Point out each leukocyte.
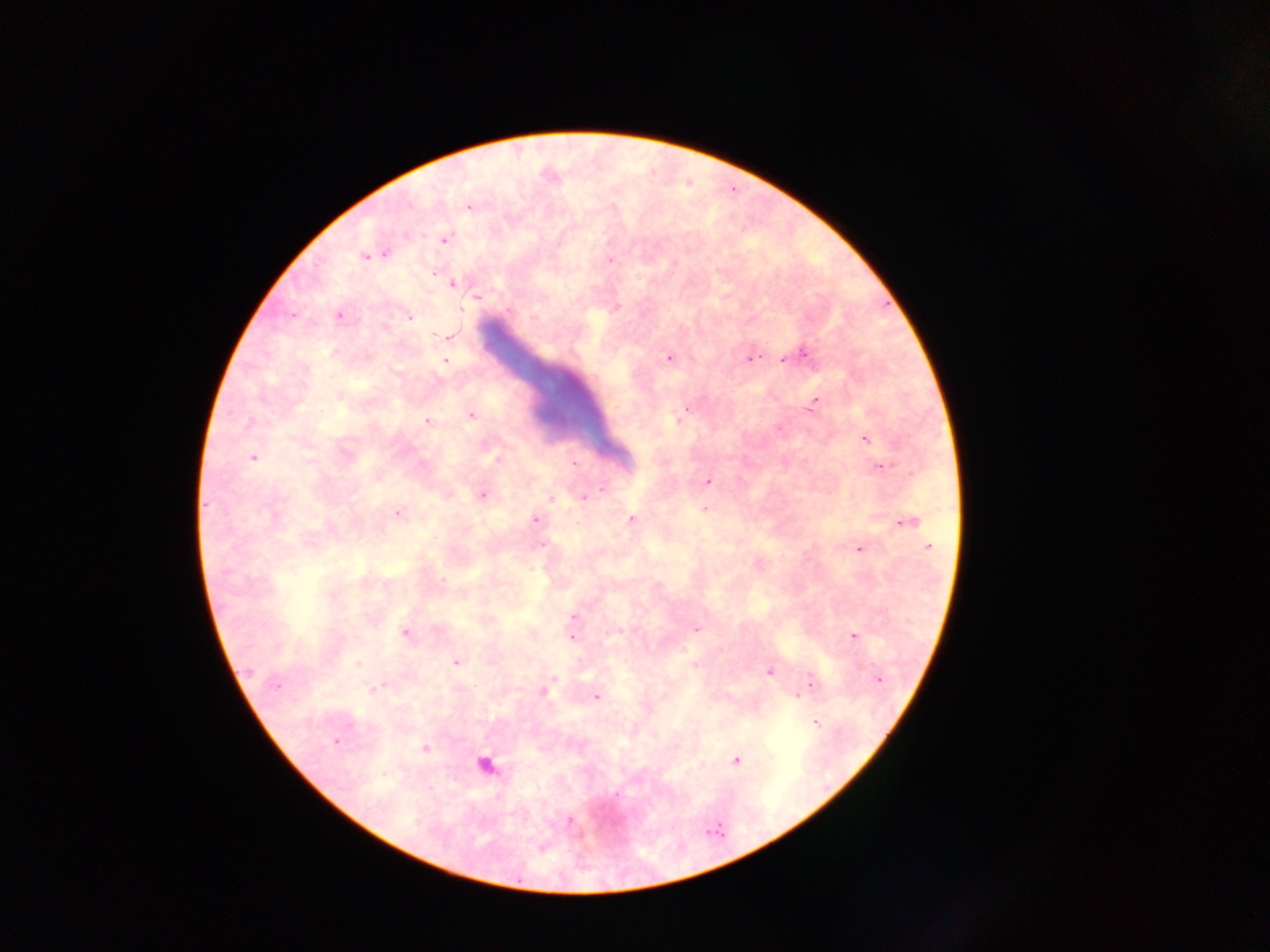

Approximate centers as [x, y] in pixels.
Leukocytes: [484, 766].

Plasmodium parasite locations = approximate centers as [x, y] in pixels: [468, 207], [444, 240], [384, 253], [365, 256], [610, 261], [434, 273], [452, 284], [477, 297], [616, 308], [461, 309], [509, 310], [292, 316], [339, 316], [409, 317], [535, 319], [447, 336], [804, 354], [668, 357], [750, 358], [783, 359], [445, 361], [340, 396], [815, 400], [687, 409], [471, 415], [681, 417], [428, 421], [677, 421], [248, 423], [865, 438], [252, 458], [497, 459], [575, 463], [882, 467], [708, 481], [601, 489], [482, 496], [584, 498], [551, 499], [704, 509], [398, 513], [274, 516], [534, 519], [632, 519], [907, 522], [541, 545], [928, 546], [859, 549], [443, 580], [574, 617], [696, 628], [404, 634], [853, 636], [572, 637], [456, 661], [358, 664], [695, 666], [250, 671], [768, 672], [554, 677], [879, 679], [810, 681], [276, 686], [377, 688], [543, 691], [797, 696], [597, 697], [816, 723], [335, 742], [425, 748], [736, 760], [617, 794], [569, 820], [541, 848]
country = Ghana
field of view = single
capture = mobile-phone photograph through a microscope
image size = 1270×952 pixels
preparation = thick blood film